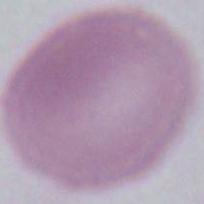
Summary:
  - Modality: micrograph
  - Identification: red blood cell
  - Magnification: 1000x